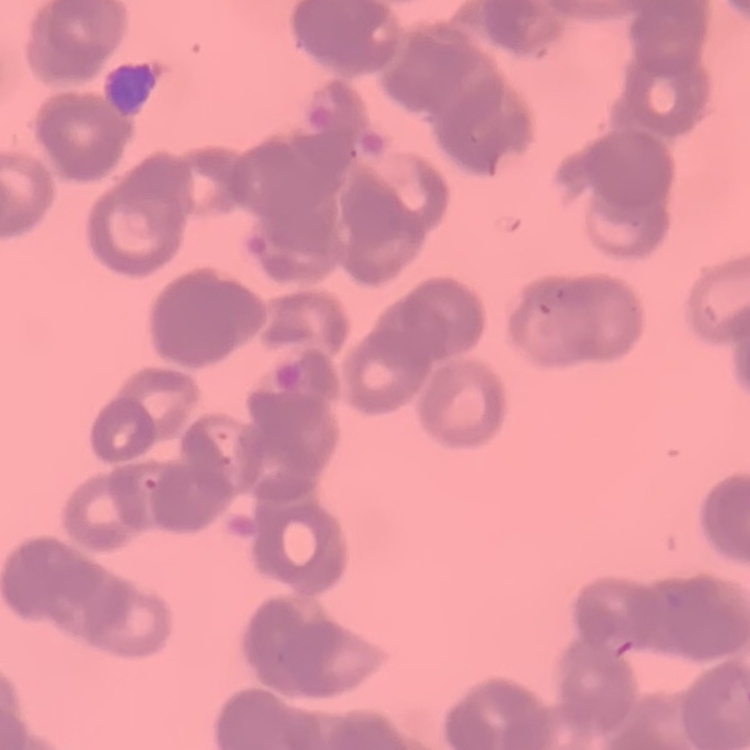

Summary:
  - Erythrocyte morphology: rouleaux formation
  - Image type: square crop of a larger photomicrograph
  - Preparation: thin blood film
  - Stain: Field's or Giemsa